Describe the morphology of the red blood cells.
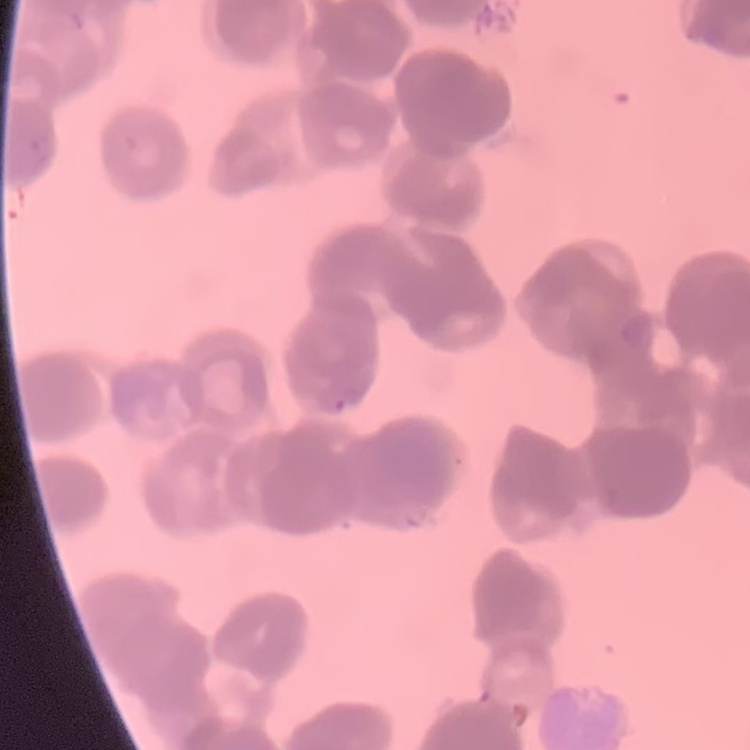
Rouleaux formation.

Thin blood film. Field's or Giemsa stain. Square crop of a larger photomicrograph.